Report the malaria status of this cell.
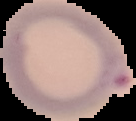
It is parasitized.

Image is 136×121 pixels. From a thin blood film. Cell region segmented out of the field of view; the surrounding area is masked to black.